Report the malaria status of this cell.
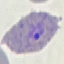
Parasitized.

Summary:
  - Capture: smartphone camera at the microscope eyepiece
  - Image type: cell patch, automatically extracted from a larger field of view and resized to 64 × 64 pixels
  - Preparation: thin blood film
  - Stain: Giemsa